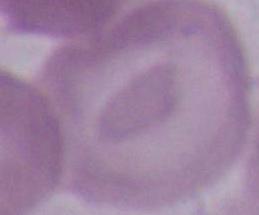

magnification = 1000x
identification = red blood cell
modality = photomicrograph